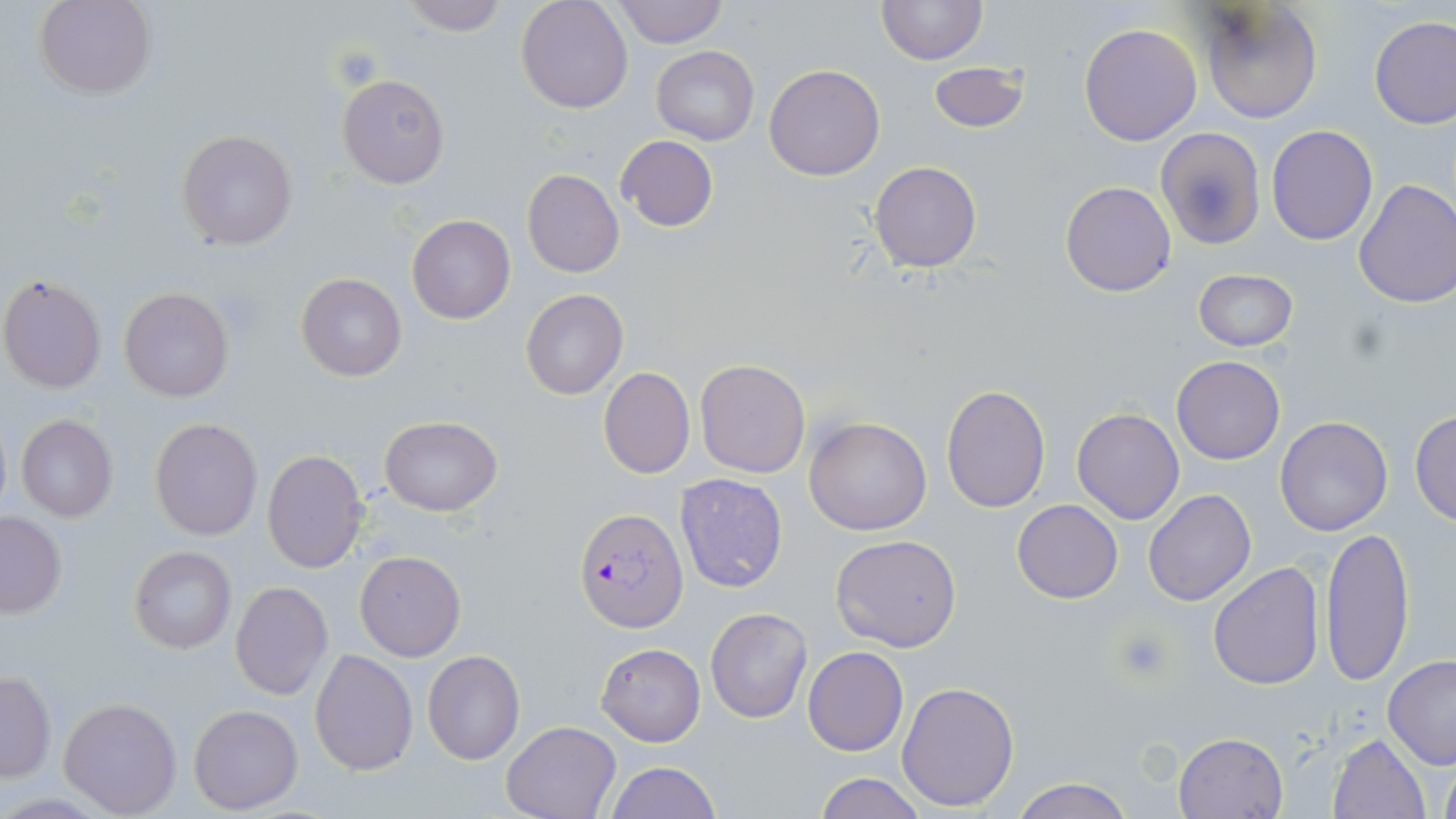

Approximate bounding boxes as [x1, y1, x2, y2] in pixels. Uninfected red blood cell locations: [36, 0, 155, 99], [400, 0, 508, 36], [515, 0, 633, 113], [611, 0, 727, 47], [877, 0, 985, 65], [1195, 2, 1322, 123], [1368, 15, 1455, 129], [1078, 23, 1203, 146], [651, 46, 759, 145], [929, 62, 1029, 132], [765, 64, 884, 182], [337, 73, 450, 189], [1267, 125, 1377, 245], [1154, 126, 1265, 250], [176, 129, 298, 250], [615, 135, 718, 231], [868, 161, 982, 272], [521, 169, 624, 278], [1354, 179, 1456, 309], [1060, 181, 1177, 297], [407, 215, 515, 324], [1192, 269, 1298, 351], [295, 272, 406, 382], [2, 274, 107, 393], [118, 285, 235, 403], [520, 288, 629, 399], [1172, 355, 1286, 465], [694, 358, 811, 478], [598, 366, 695, 479], [940, 385, 1051, 512], [1072, 408, 1185, 524], [1409, 410, 1456, 525], [16, 414, 118, 522], [377, 416, 503, 517], [1275, 417, 1393, 536], [804, 418, 931, 537], [149, 419, 263, 540], [261, 449, 369, 574], [675, 473, 788, 593], [1143, 490, 1255, 606], [1011, 499, 1124, 603], [0, 512, 67, 617], [1319, 525, 1414, 687], [830, 534, 961, 652], [130, 545, 236, 654], [354, 550, 467, 661], [1208, 561, 1325, 689], [230, 581, 333, 700], [705, 607, 813, 724], [595, 643, 705, 747], [803, 646, 908, 756], [310, 648, 418, 775], [423, 650, 526, 764], [1382, 655, 1456, 768], [0, 672, 56, 783], [896, 680, 1019, 812], [58, 696, 183, 817], [189, 704, 304, 813], [501, 720, 620, 819], [1174, 732, 1288, 819], [1327, 732, 1431, 819], [1437, 758, 1456, 819], [605, 761, 722, 819], [814, 773, 928, 819], [1010, 777, 1132, 819]. Platelet locations: [330, 45, 383, 90], [1111, 629, 1174, 682]. Plasmodium falciparum-infected red blood cell locations: [576, 508, 688, 630]. Slide-level diagnosis: Plasmodium falciparum. Captured at 1000x magnification. Image is 1456×819 pixels. One field of a larger specimen. Thin blood smear. May-Grünwald-Giemsa-stained preparation. Light microscopy.